Report the malaria status of this cell.
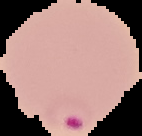
Parasitized.

{
  "image_size": "142×136 pixels",
  "image_type": "segmented cell region on a black background",
  "preparation": "thin blood film"
}